Locate every Plasmodium parasite.
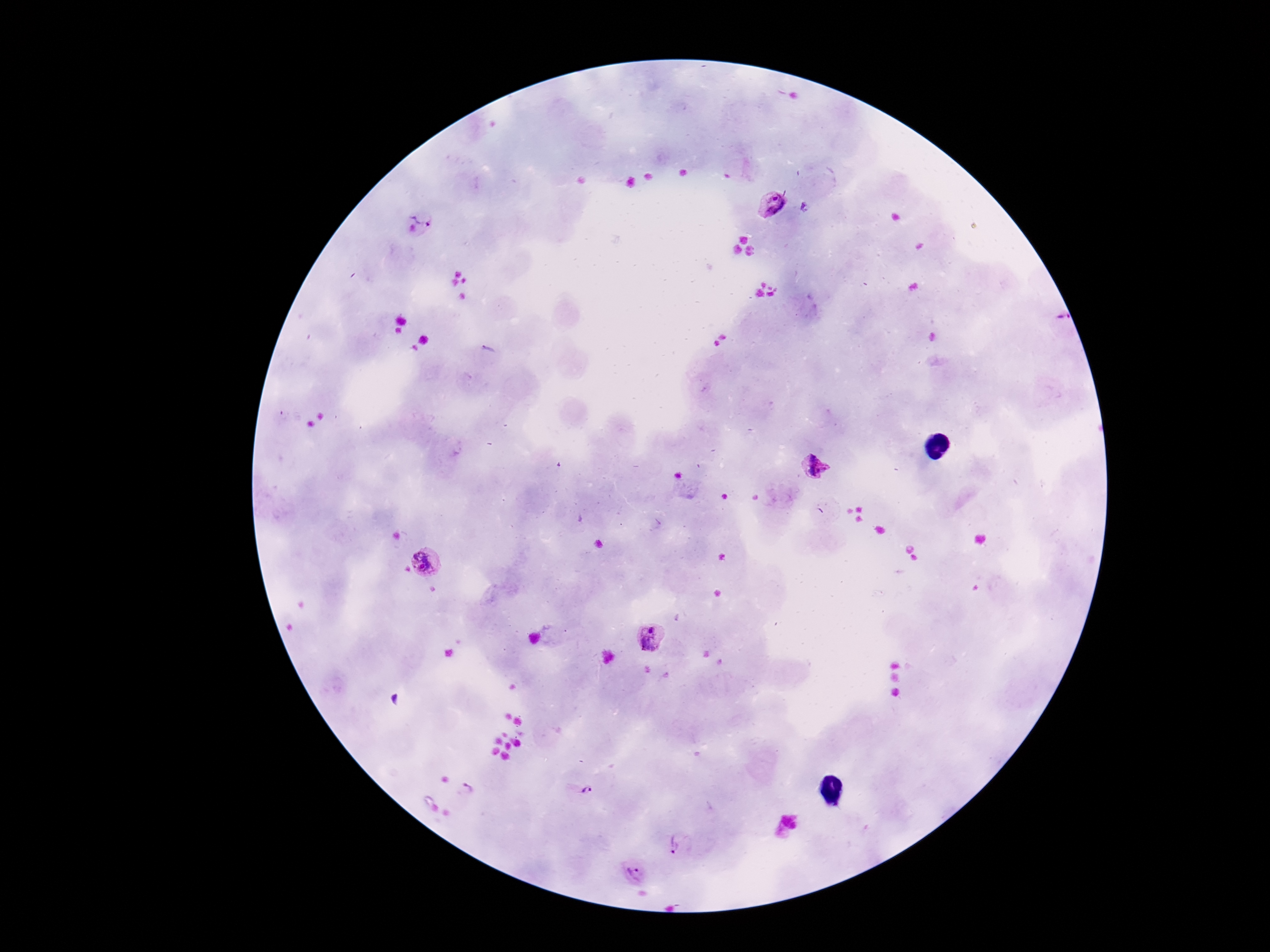

Approximate centers as (x, y) in pixels.
Plasmodium parasites: (772, 204), (425, 209), (487, 351), (814, 466), (425, 562), (651, 638), (467, 788), (579, 790), (678, 846), (635, 873).

capture = smartphone camera through the microscope eyepiece
magnification = 100x
preparation = thick blood smear
patient malaria status = positive
field of view = one from this slide
stain = Giemsa
image size = 1270×952 pixels